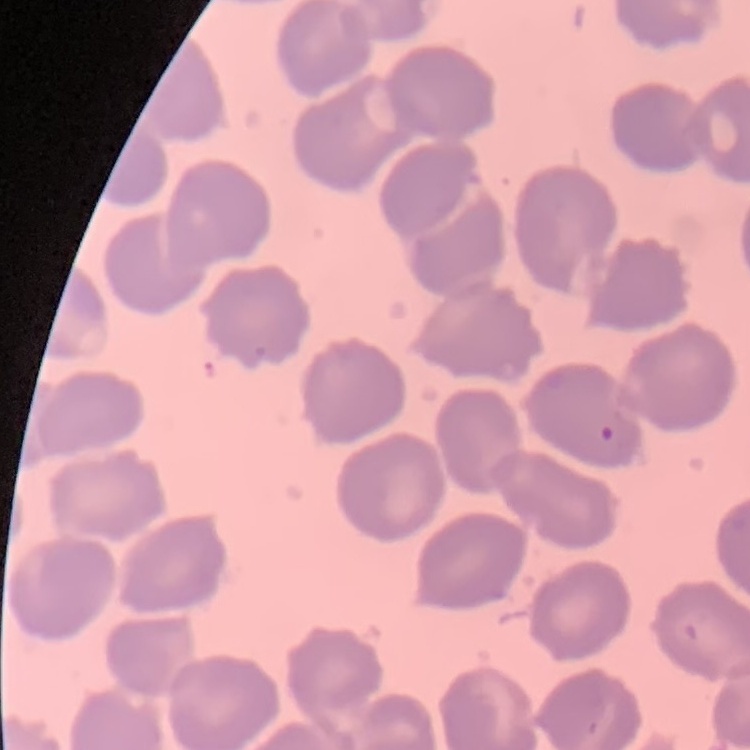

Summary:
  - Red blood cell morphology: no rouleaux formation
  - Preparation: thin peripheral smear
  - Stain: Field's or Giemsa
  - Image type: square crop of a larger photomicrograph